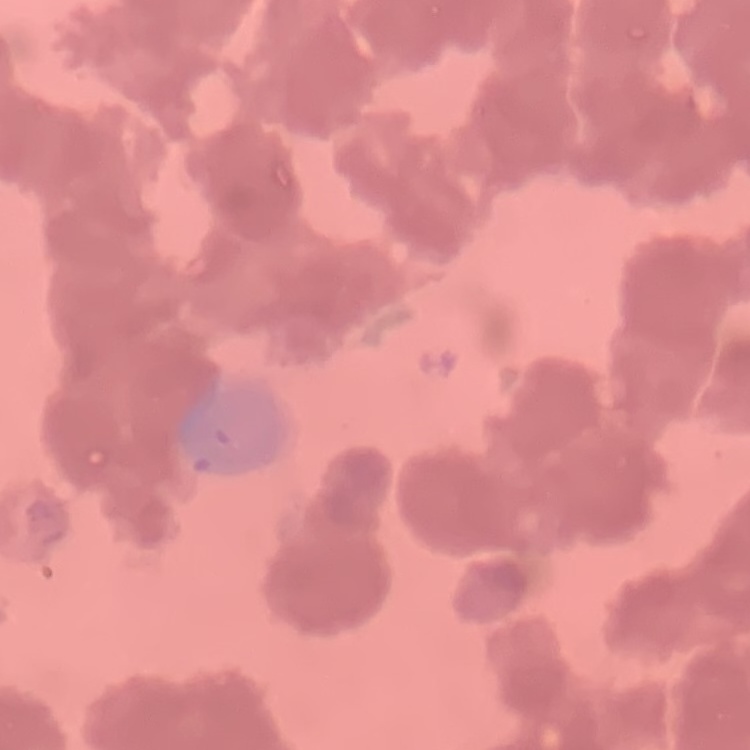
red blood cell morphology = rouleaux formation
image type = one tile cut from a larger photomicrograph
stain = Field's or Giemsa
preparation = thin blood smear